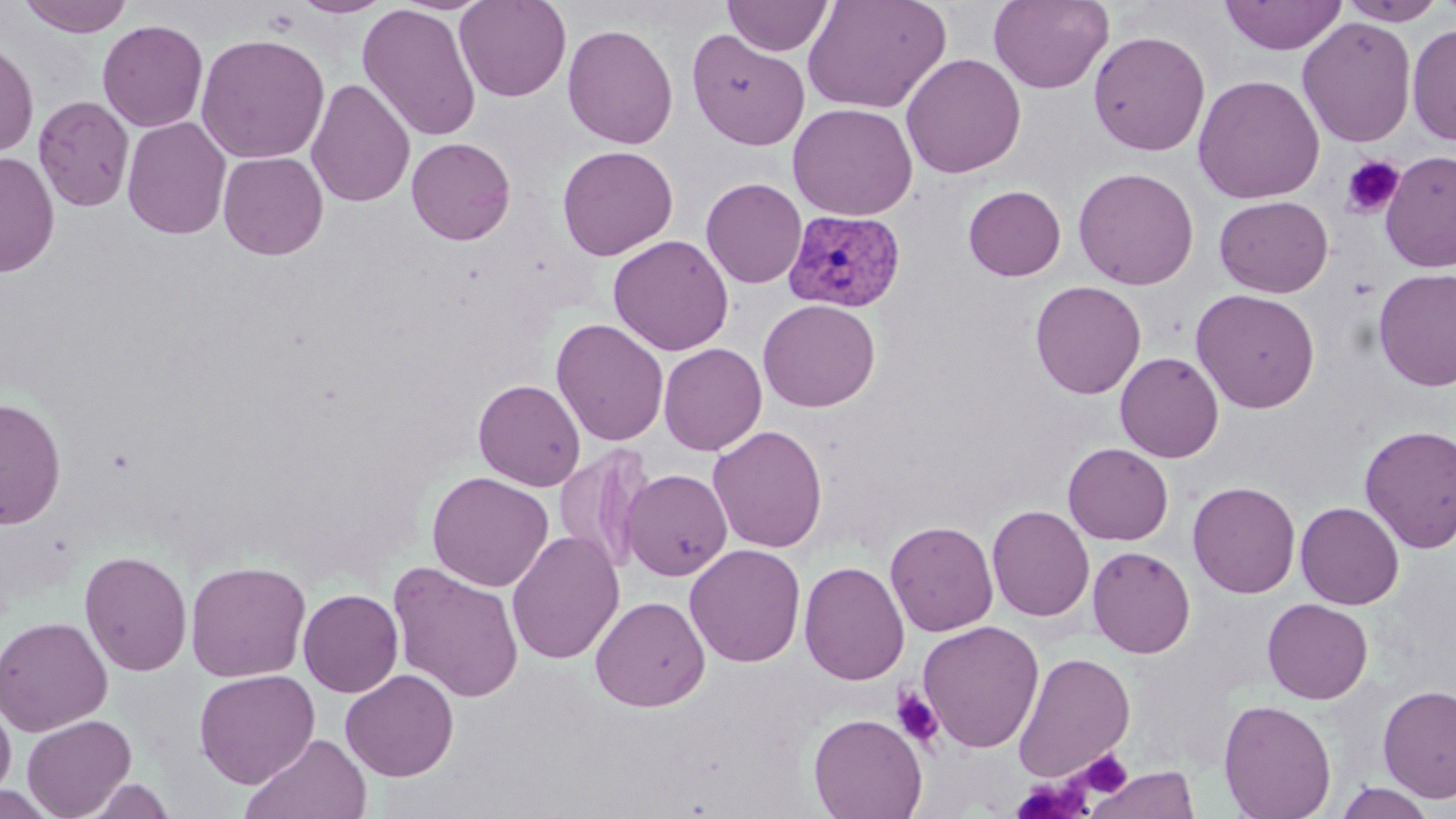

{
  "slide_level_diagnosis": "Plasmodium vivax",
  "image_size": "1456×819 pixels",
  "stain": "May-Grünwald-Giemsa",
  "field_of_view": "single",
  "uninfected_red_blood_cell_locations": "approximate bounding boxes as (x1, y1, x2, y2) in pixels: (19, 0, 135, 37), (291, 0, 393, 18), (454, 0, 572, 102), (724, 0, 833, 56), (802, 0, 951, 115), (988, 0, 1113, 93), (1219, 0, 1347, 55), (1337, 1, 1447, 25), (357, 3, 482, 143), (1297, 17, 1417, 148), (97, 19, 208, 133), (562, 23, 678, 149), (1406, 23, 1456, 146), (687, 29, 810, 150), (1088, 30, 1211, 156), (195, 32, 330, 165), (0, 39, 39, 158), (901, 52, 1026, 179), (1192, 74, 1325, 205), (306, 78, 415, 208), (33, 96, 134, 212), (788, 102, 918, 220), (122, 117, 231, 240), (406, 137, 516, 245), (557, 145, 678, 261), (218, 151, 328, 260), (1380, 151, 1456, 272), (1, 152, 59, 277), (1073, 167, 1199, 290), (700, 177, 807, 288), (963, 185, 1066, 281), (1214, 195, 1334, 297), (608, 234, 734, 356), (1373, 267, 1456, 392), (1030, 280, 1147, 398), (1191, 288, 1320, 414), (757, 298, 881, 412), (551, 317, 669, 447), (658, 342, 767, 455), (1115, 351, 1224, 463), (473, 379, 586, 491), (0, 397, 66, 530), (708, 424, 828, 553), (1359, 424, 1456, 554), (1063, 442, 1173, 545), (553, 444, 656, 575), (622, 468, 732, 580), (427, 471, 553, 592), (1187, 480, 1301, 598), (1295, 501, 1404, 609), (986, 504, 1095, 622), (885, 520, 999, 637), (506, 530, 625, 664), (684, 543, 806, 668), (1087, 545, 1195, 658), (78, 550, 193, 676), (798, 560, 910, 685), (185, 561, 311, 682), (388, 561, 525, 703), (298, 588, 404, 697), (590, 595, 710, 711), (1262, 598, 1373, 704), (0, 616, 113, 736), (917, 620, 1044, 753), (1013, 651, 1136, 781), (194, 669, 320, 788), (340, 669, 459, 781), (1377, 684, 1456, 803), (0, 696, 16, 799), (1218, 698, 1337, 819), (808, 713, 927, 819), (22, 714, 137, 819), (241, 733, 372, 819), (1085, 765, 1200, 819), (79, 777, 179, 818), (1333, 782, 1437, 819)",
  "modality": "optical microscopy",
  "plasmodium_vivax_infected_red_blood_cell_locations": "approximate bounding boxes as (x1, y1, x2, y2) in pixels: (779, 210, 905, 313)",
  "magnification": "1000x",
  "platelet_locations": "approximate bounding boxes as (x1, y1, x2, y2) in pixels: (1341, 155, 1405, 219), (892, 689, 944, 748), (1076, 750, 1132, 799), (1011, 777, 1093, 819)",
  "preparation": "thin blood smear"
}